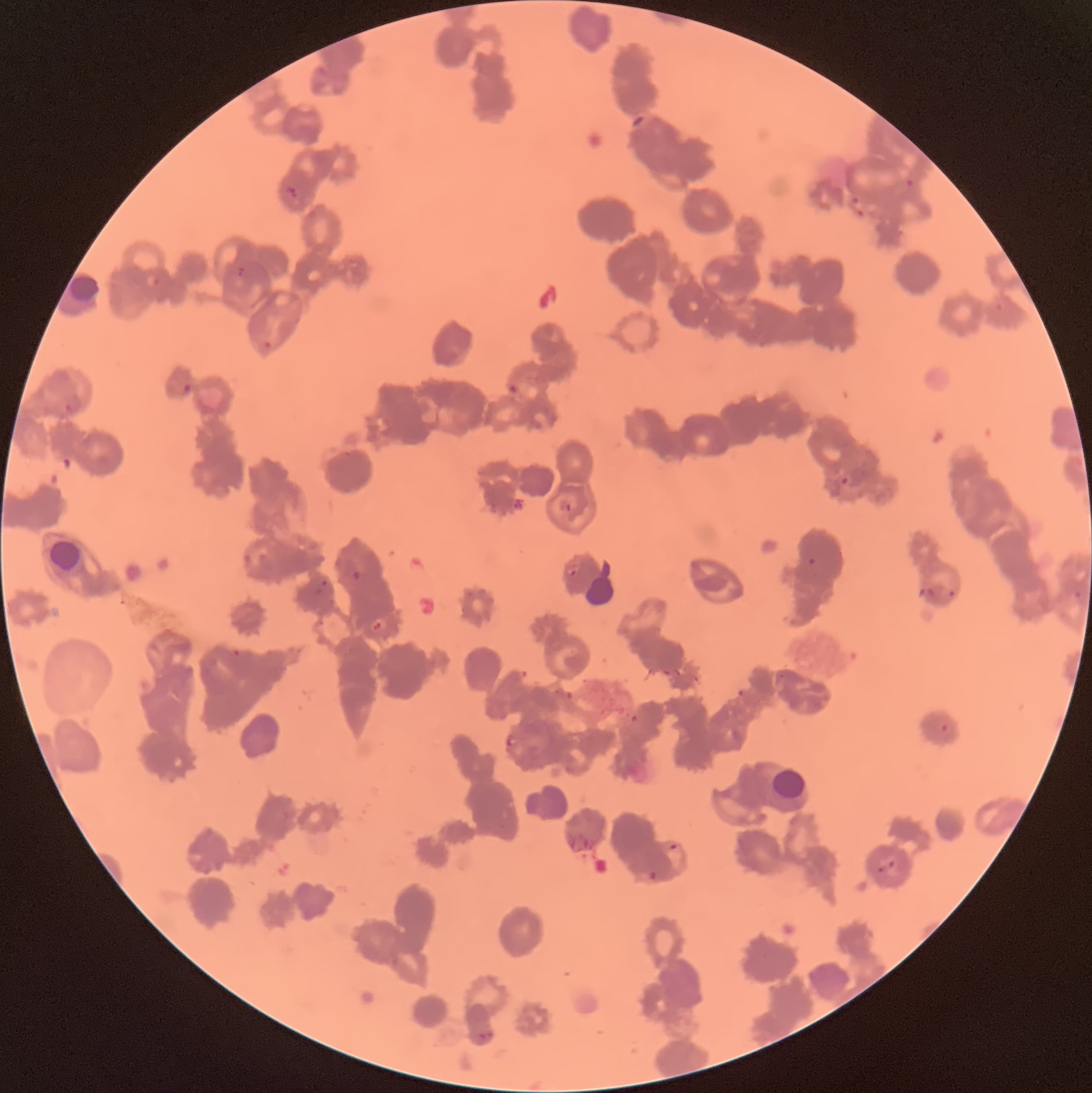

{
  "preparation": "thin blood film",
  "plasmodium_parasite_locations": "approximate bounding boxes as (x1,y1)-(x2,y2) corner pairs in pixels: (631,114)-(645,127), (904,177)-(916,189), (286,184)-(298,201), (849,196)-(866,219), (237,266)-(245,276), (144,271)-(162,287), (259,340)-(271,350), (182,382)-(192,393), (505,382)-(522,397), (65,402)-(72,414), (840,476)-(850,485), (564,503)-(573,513), (334,554)-(363,582), (808,556)-(817,566), (567,567)-(579,577), (315,580)-(332,597), (916,586)-(939,600), (947,589)-(956,598), (1073,589)-(1084,601), (371,617)-(387,632), (230,647)-(243,659), (736,689)-(745,697), (566,690)-(575,700), (630,714)-(640,723), (940,722)-(950,733), (504,736)-(518,748), (566,832)-(594,854), (667,843)-(679,852), (877,859)-(895,872), (647,870)-(657,882), (475,1031)-(494,1044)",
  "modality": "optical microscopy",
  "image_size": "1092×1093 pixels",
  "red_blood_cell_morphology": "rouleaux formation"
}